Assess this cell for malaria.
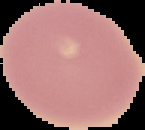

Uninfected.

Cell region segmented out of the field of view; the surrounding area is masked to black. From a thin blood film. Image is 145×130 pixels.